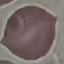

Summary:
  - Result: no malaria parasites detected
  - Preparation: thin smear
  - Image type: automatically extracted cell patch, resized to 64 × 64 pixels
  - Capture: smartphone camera at the microscope eyepiece
  - Stain: Giemsa